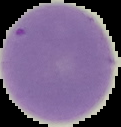
result = no Plasmodium parasites detected
image size = 121×127 pixels
image type = segmented cell region with the area outside set to black
preparation = thin blood film